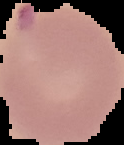
Image is 124×145 pixels. From a thin blood film. Result: malaria parasites detected. The area outside the segmented cell region is set to black.